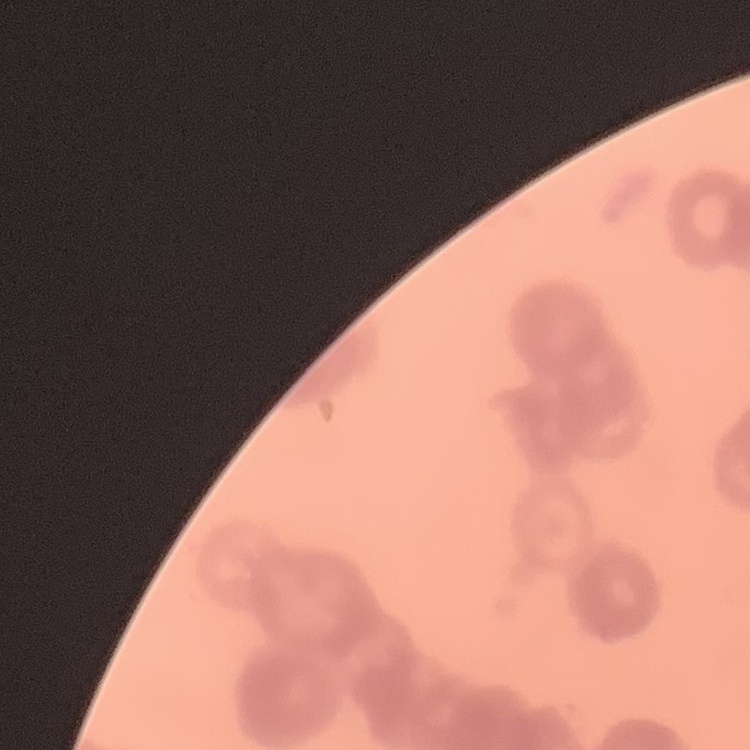
Summary:
  - Erythrocyte morphology: rouleaux formation
  - Preparation: thin peripheral smear
  - Image type: square crop of a larger photomicrograph
  - Stain: Field's or Giemsa